Describe the morphology of the erythrocytes.
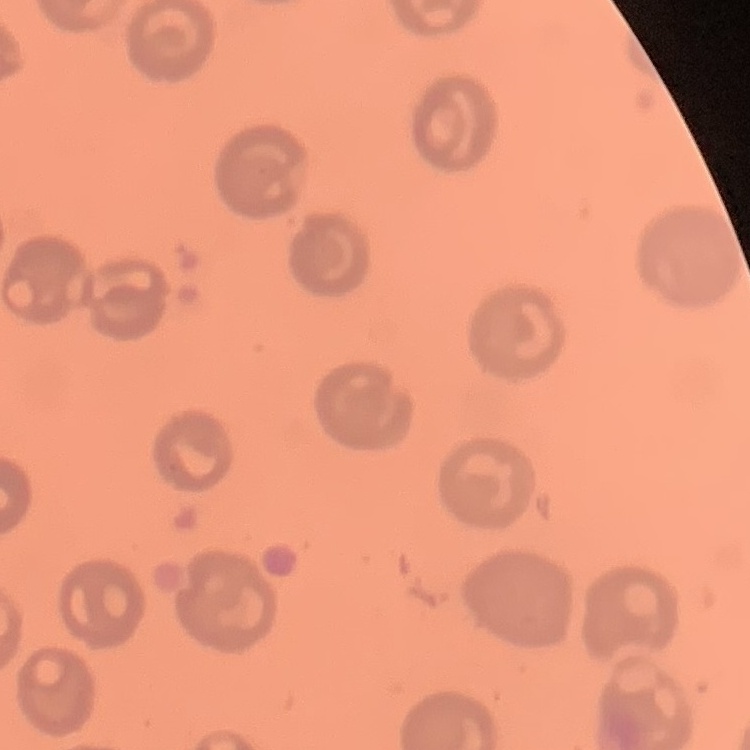

They show no rouleaux formation.

Summary:
  - Stain: Field's or Giemsa
  - Preparation: thin peripheral smear
  - Image type: square crop of a larger photomicrograph